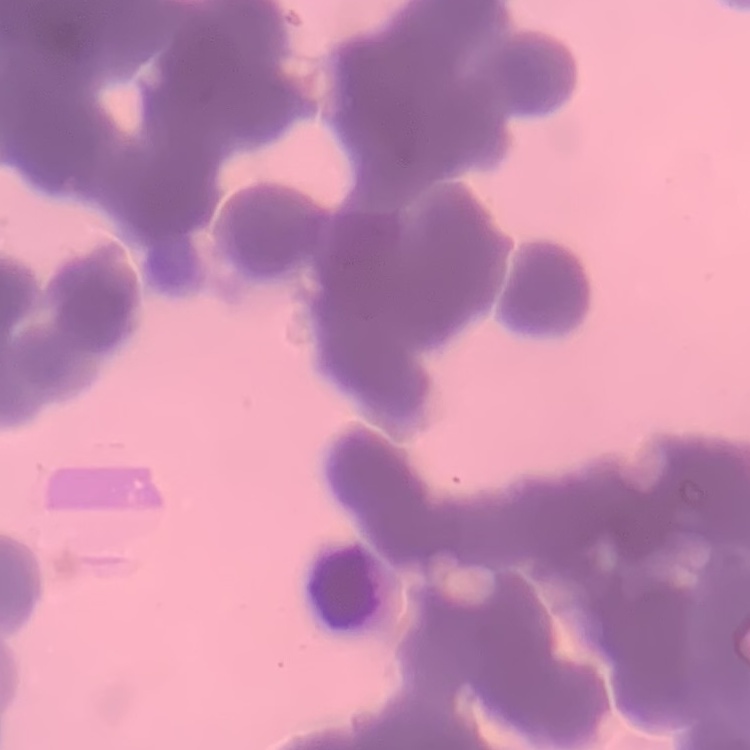
The erythrocytes exhibit rouleaux formation. One tile cut from a larger photomicrograph. Thin peripheral smear. Stained with either Field's or Giemsa.